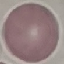

result = negative for malaria parasites
image type = cell patch, automatically extracted from a larger field of view and resized to 64 × 64 pixels
preparation = thin blood film
stain = Giemsa
capture = smartphone through the microscope eyepiece